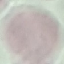
result = no malaria parasites detected
capture = smartphone camera at the microscope eyepiece
image type = automatically extracted cell patch, resized to 64 × 64 pixels
stain = Giemsa
preparation = thin blood smear